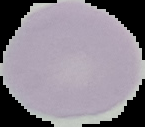
{
  "image_size": "145×127 pixels",
  "preparation": "thin blood smear",
  "malaria_status": "uninfected",
  "image_type": "segmented cell region on a black background"
}